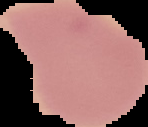
Summary:
  - Preparation: thin blood film
  - Result: no Plasmodium parasites seen
  - Image size: 148×127 pixels
  - Image type: cell region segmented out of the field of view; surrounding area masked to black